Locate every blood parasite and identify its species.
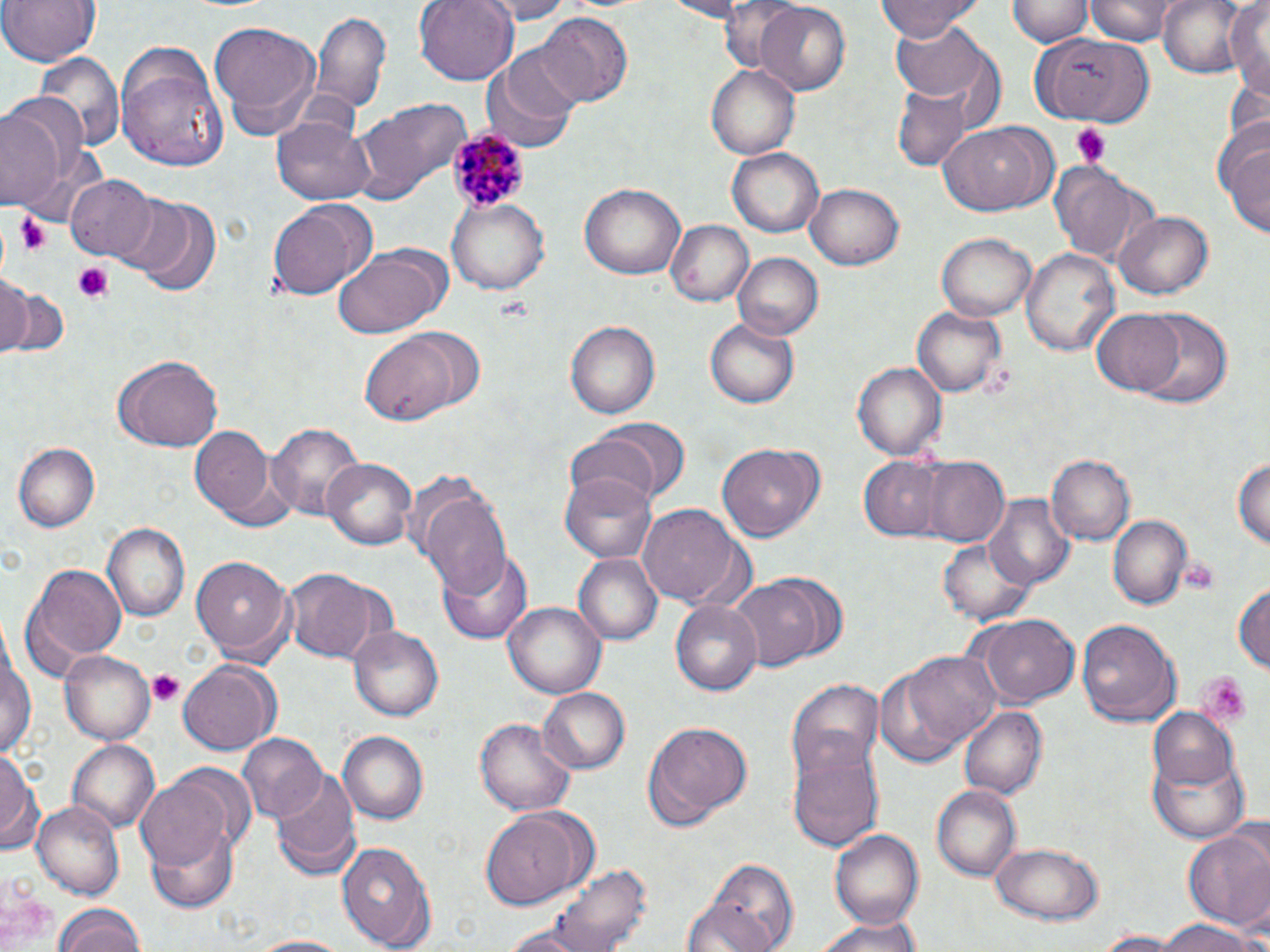
Approximate bounding boxes as (x1, y1, x2, y2) in pixels.
Plasmodium malariae-infected red blood cells: (447, 127, 536, 219).
No Plasmodium falciparum, Plasmodium ovale, Plasmodium vivax, Babesia divergens, or Trypanosoma brucei observed.

Summary:
  - Uninfected red blood cell locations: (0, 0, 100, 67), (415, 0, 517, 84), (476, 0, 579, 23), (654, 0, 757, 19), (877, 0, 983, 41), (1007, 0, 1092, 46), (1086, 0, 1176, 43), (1157, 0, 1256, 81), (1223, 0, 1269, 91), (712, 1, 807, 74), (754, 4, 850, 94), (312, 7, 393, 118), (539, 13, 631, 105), (889, 17, 999, 115), (209, 21, 321, 136), (1029, 36, 1146, 120), (114, 44, 227, 170), (485, 47, 582, 154), (36, 52, 124, 156), (706, 62, 800, 157), (893, 86, 970, 171), (350, 96, 473, 206), (0, 106, 64, 210), (272, 116, 377, 205), (937, 123, 1049, 216), (1220, 130, 1270, 240), (728, 149, 823, 238), (1052, 165, 1136, 260), (65, 173, 156, 260), (580, 182, 687, 281), (806, 182, 904, 269), (123, 195, 222, 296), (449, 198, 549, 294), (268, 200, 371, 301), (1114, 211, 1214, 300), (664, 219, 753, 307), (937, 233, 1036, 321), (332, 245, 450, 337), (1021, 246, 1119, 355), (734, 252, 823, 340), (0, 272, 31, 357), (2, 282, 67, 356), (910, 306, 1007, 398), (1131, 307, 1233, 413), (1090, 309, 1186, 396), (706, 317, 799, 407), (564, 319, 661, 419), (361, 326, 484, 426), (113, 353, 225, 453), (852, 362, 945, 461), (569, 420, 685, 511), (265, 421, 364, 523), (188, 426, 276, 520), (12, 441, 101, 532), (718, 442, 821, 541), (1233, 454, 1269, 555), (1046, 455, 1133, 546), (859, 456, 948, 540), (324, 457, 416, 550), (919, 458, 1010, 545), (560, 470, 657, 566), (415, 484, 513, 592), (981, 494, 1076, 587), (638, 503, 745, 605), (1108, 514, 1193, 610), (101, 522, 191, 623), (937, 537, 1041, 625), (436, 548, 533, 644), (574, 552, 662, 644), (193, 555, 294, 661), (22, 560, 125, 676), (285, 569, 386, 663), (728, 577, 824, 672), (1233, 579, 1269, 679), (671, 598, 763, 697), (504, 603, 604, 697), (973, 613, 1078, 705), (1075, 618, 1178, 725), (0, 619, 34, 763), (349, 624, 444, 721), (875, 648, 1003, 765), (61, 650, 154, 745), (178, 661, 279, 756), (784, 677, 886, 791), (538, 688, 629, 774), (960, 706, 1046, 800), (1149, 707, 1241, 794), (475, 719, 576, 815), (645, 722, 752, 826), (338, 730, 430, 824), (235, 733, 325, 821), (69, 739, 160, 832), (787, 745, 883, 855), (0, 747, 41, 853), (1151, 752, 1249, 843), (271, 773, 360, 881), (136, 775, 233, 871), (931, 786, 1021, 883), (33, 801, 125, 900), (481, 807, 593, 908), (147, 822, 239, 912), (1184, 827, 1270, 934), (831, 828, 922, 929), (339, 840, 435, 951), (988, 841, 1106, 925), (704, 858, 799, 952), (547, 862, 652, 951), (53, 906, 149, 951), (807, 916, 929, 952), (1151, 919, 1260, 952), (1094, 932, 1190, 951), (244, 936, 355, 952)
  - Platelet locations: (1069, 122, 1113, 167), (17, 212, 51, 256), (72, 261, 114, 301), (1183, 563, 1215, 594), (147, 669, 185, 708), (1195, 670, 1253, 726)
  - Slide-level diagnosis: Plasmodium malariae
  - Modality: light microscopy
  - Stain: May-Grünwald-Giemsa
  - Image size: 1270×952 pixels
  - Magnification: 1000x
  - Preparation: thin blood smear
  - Field of view: one of a larger specimen